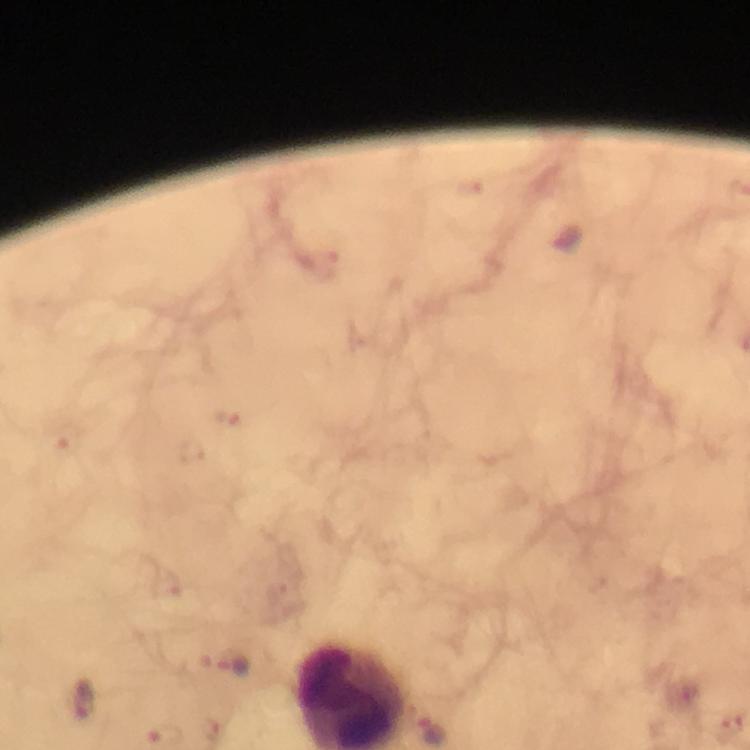

image size = 750×750 pixels
context = from a diagnostic examination for malaria
capture = smartphone photograph through a microscope
preparation = thick smear
cropped from = a single field of view
Plasmodium parasite locations = approximate centers as [x, y] in pixels: [227, 416], [65, 436], [192, 449], [164, 584], [225, 665], [83, 702]
immersion oil = applied
stain = Giemsa
magnification = 100x